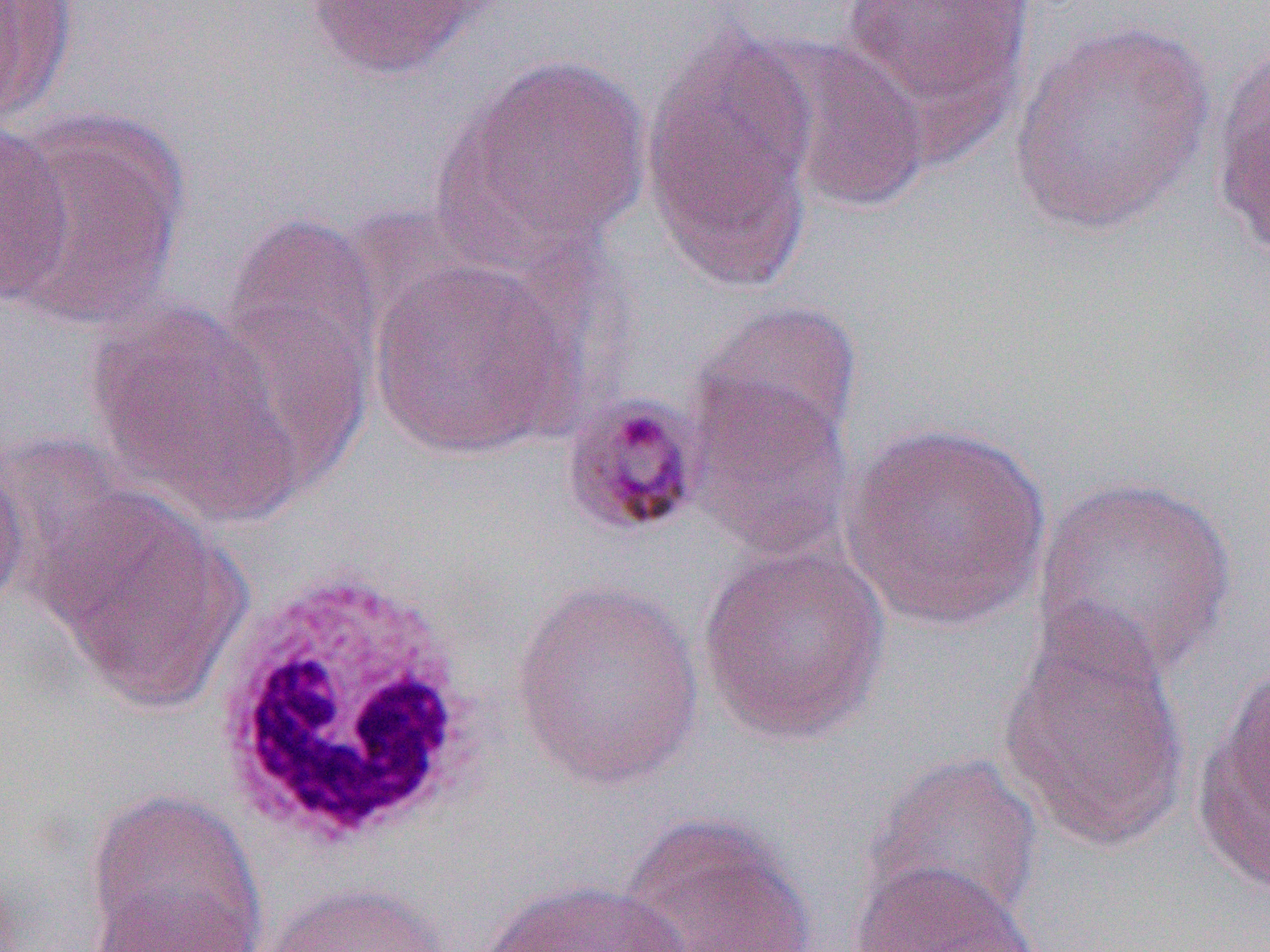 Approximate bounding boxes as (x1, y1, x2, y2) in pixels. Uninfected red blood cell locations: (0, 1, 77, 125), (303, 1, 490, 80), (838, 1, 1034, 129), (641, 18, 821, 290), (1010, 18, 1214, 238), (755, 32, 931, 216), (1209, 39, 1270, 263), (440, 54, 653, 261), (0, 110, 184, 328), (0, 123, 72, 308), (216, 201, 385, 455), (368, 254, 579, 459), (85, 300, 305, 522), (690, 300, 863, 457), (685, 373, 855, 564), (837, 421, 1054, 631), (0, 448, 29, 621), (1031, 476, 1239, 682), (43, 491, 248, 712), (696, 542, 893, 745), (510, 578, 708, 790), (997, 606, 1192, 853), (1192, 664, 1270, 893), (862, 751, 1045, 932), (85, 791, 266, 952), (618, 811, 818, 952), (848, 859, 1041, 952), (87, 879, 266, 951), (474, 879, 694, 951), (261, 883, 453, 952). White blood cell locations: (209, 561, 489, 852). Slide-level diagnosis: Plasmodium malariae. Thin blood film. 1000x magnification. Image is 1270×952 pixels. Light microscopy. Single field of view.